Comment on the background quality.
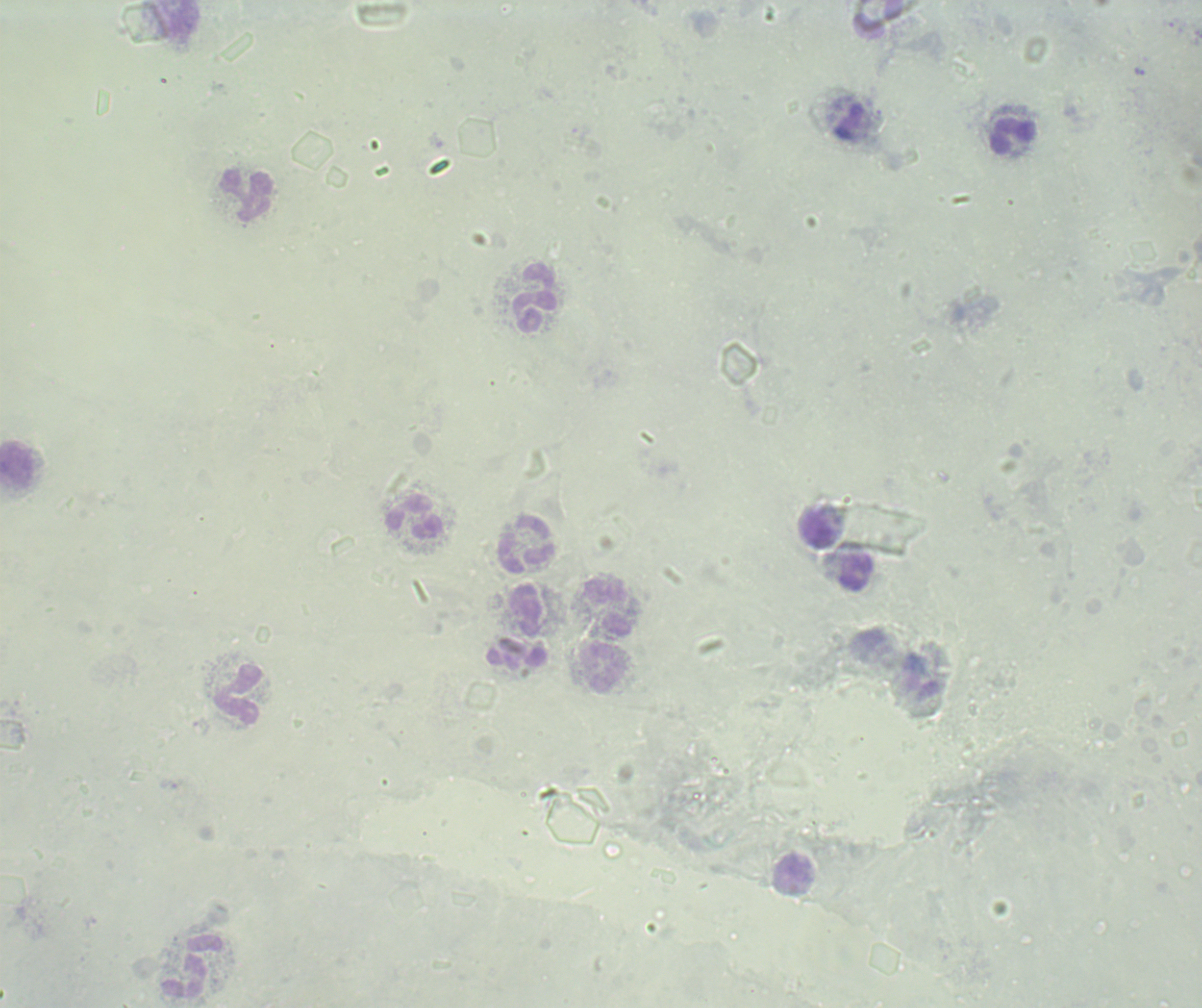

Unsatisfactory.

Approximate object centers, in pixels from the top-left corner. Leukocyte locations: (x=181, y=20), (x=849, y=123), (x=1013, y=135), (x=248, y=195), (x=535, y=299), (x=17, y=465), (x=415, y=517), (x=818, y=528), (x=526, y=545), (x=856, y=571), (x=609, y=608), (x=528, y=611), (x=518, y=659), (x=604, y=668), (x=238, y=696), (x=794, y=876), (x=194, y=967). Thick blood film. Result: no malaria parasites seen. Image is 1202×1008 pixels. Single field of view. Previously used in an actual diagnosis. Romanowsky stain. Captured at 100x magnification.